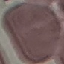
Result: no malaria parasites seen. Photographed with a smartphone camera at the microscope eyepiece. Cell patch, automatically extracted from a larger field of view and resized to 64 × 64 pixels. Thin blood smear. Giemsa-stained preparation.